Assess this cell for malaria.
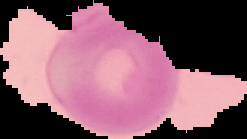
It is uninfected.

Segmented cell region on a black background. From a thin blood smear. Image is 247×139 pixels.